Mark where platelets are.
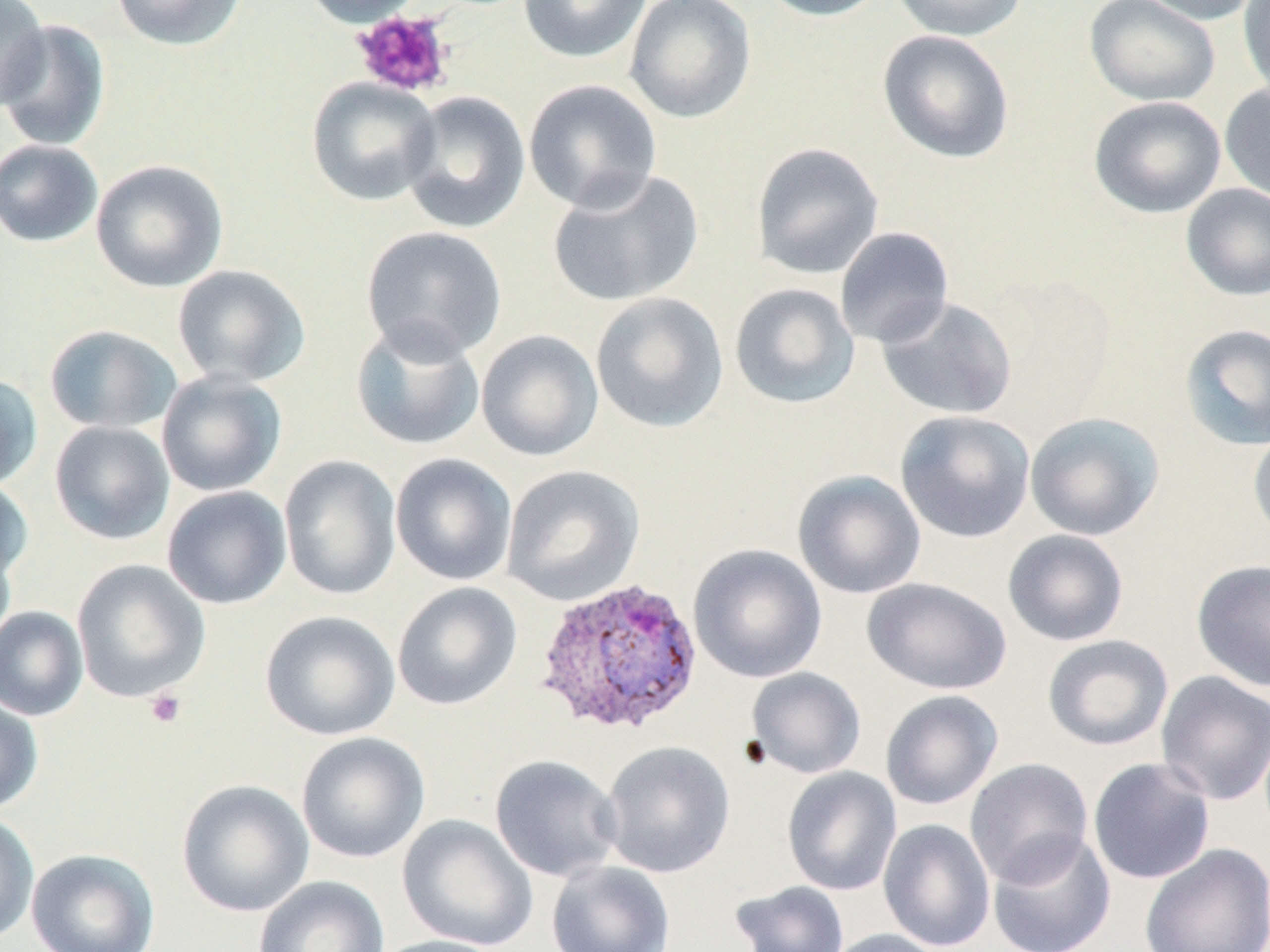
Approximate bounding boxes as named x1/y1/x2/y2 corners in pixels.
Platelets: (x1=350, y1=10, x2=456, y2=98), (x1=144, y1=689, x2=188, y2=729).

Plasmodium vivax-infected red blood cell locations: (x1=534, y1=577, x2=704, y2=737). Uninfected red blood cell locations: (x1=0, y1=0, x2=51, y2=110), (x1=110, y1=0, x2=248, y2=51), (x1=299, y1=0, x2=428, y2=27), (x1=518, y1=0, x2=651, y2=63), (x1=623, y1=0, x2=757, y2=124), (x1=757, y1=0, x2=890, y2=21), (x1=892, y1=0, x2=1028, y2=42), (x1=1134, y1=0, x2=1262, y2=26), (x1=1238, y1=0, x2=1270, y2=100), (x1=1084, y1=1, x2=1221, y2=107), (x1=0, y1=18, x2=111, y2=152), (x1=877, y1=30, x2=1015, y2=164), (x1=306, y1=77, x2=441, y2=206), (x1=523, y1=78, x2=663, y2=214), (x1=1219, y1=82, x2=1270, y2=202), (x1=401, y1=91, x2=530, y2=234), (x1=1088, y1=96, x2=1227, y2=218), (x1=0, y1=139, x2=104, y2=248), (x1=751, y1=142, x2=885, y2=280), (x1=90, y1=159, x2=229, y2=292), (x1=546, y1=168, x2=705, y2=308), (x1=1181, y1=183, x2=1270, y2=301), (x1=361, y1=225, x2=508, y2=363), (x1=834, y1=227, x2=954, y2=349), (x1=172, y1=264, x2=311, y2=389), (x1=729, y1=282, x2=860, y2=410), (x1=590, y1=292, x2=729, y2=433), (x1=877, y1=296, x2=1017, y2=420), (x1=350, y1=320, x2=485, y2=451), (x1=1179, y1=323, x2=1270, y2=451), (x1=44, y1=324, x2=182, y2=434), (x1=475, y1=329, x2=604, y2=462), (x1=156, y1=369, x2=287, y2=497), (x1=0, y1=373, x2=43, y2=491), (x1=895, y1=410, x2=1036, y2=543), (x1=1024, y1=412, x2=1165, y2=541), (x1=49, y1=421, x2=174, y2=545), (x1=1248, y1=427, x2=1270, y2=544), (x1=390, y1=453, x2=518, y2=586), (x1=278, y1=454, x2=401, y2=600), (x1=501, y1=464, x2=645, y2=607), (x1=792, y1=469, x2=926, y2=599), (x1=0, y1=477, x2=33, y2=583), (x1=161, y1=485, x2=293, y2=610), (x1=1002, y1=529, x2=1129, y2=646), (x1=0, y1=534, x2=16, y2=651), (x1=688, y1=544, x2=828, y2=683), (x1=71, y1=559, x2=210, y2=703), (x1=1190, y1=559, x2=1270, y2=691), (x1=862, y1=577, x2=1012, y2=695), (x1=392, y1=581, x2=523, y2=711), (x1=0, y1=606, x2=89, y2=721), (x1=259, y1=610, x2=401, y2=741), (x1=1042, y1=634, x2=1174, y2=751), (x1=747, y1=667, x2=866, y2=779), (x1=1155, y1=670, x2=1270, y2=806), (x1=880, y1=690, x2=1003, y2=810), (x1=0, y1=694, x2=44, y2=815), (x1=296, y1=732, x2=430, y2=864), (x1=600, y1=740, x2=735, y2=878), (x1=489, y1=754, x2=623, y2=882), (x1=964, y1=757, x2=1094, y2=887), (x1=1087, y1=757, x2=1216, y2=885), (x1=781, y1=766, x2=902, y2=896), (x1=176, y1=778, x2=314, y2=917), (x1=0, y1=812, x2=39, y2=944), (x1=397, y1=814, x2=538, y2=951), (x1=878, y1=818, x2=995, y2=951), (x1=988, y1=831, x2=1116, y2=952), (x1=1139, y1=842, x2=1270, y2=952), (x1=26, y1=848, x2=160, y2=952), (x1=546, y1=860, x2=676, y2=952), (x1=254, y1=876, x2=390, y2=952), (x1=729, y1=880, x2=851, y2=952), (x1=824, y1=928, x2=950, y2=952), (x1=369, y1=935, x2=511, y2=952). Slide-level diagnosis: Plasmodium vivax. 1000x magnification. Thin blood film. Image is 1270×952 pixels. One field of a larger specimen. Optical microscopy. May-Grünwald-Giemsa-stained preparation.